State which cell type is depicted.
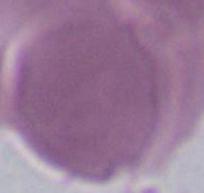
An erythrocyte.

modality = photomicrograph
magnification = 1000x